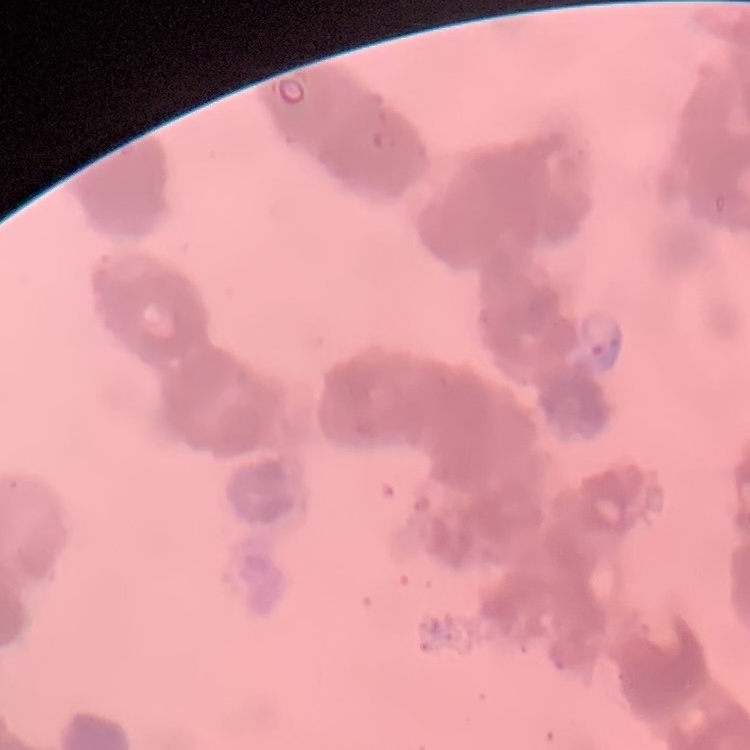

The red blood cells exhibit rouleaux formation. Thin blood smear. Stained with either Field's or Giemsa. Square crop of a larger photomicrograph.